Give the position of every malaria parasite.
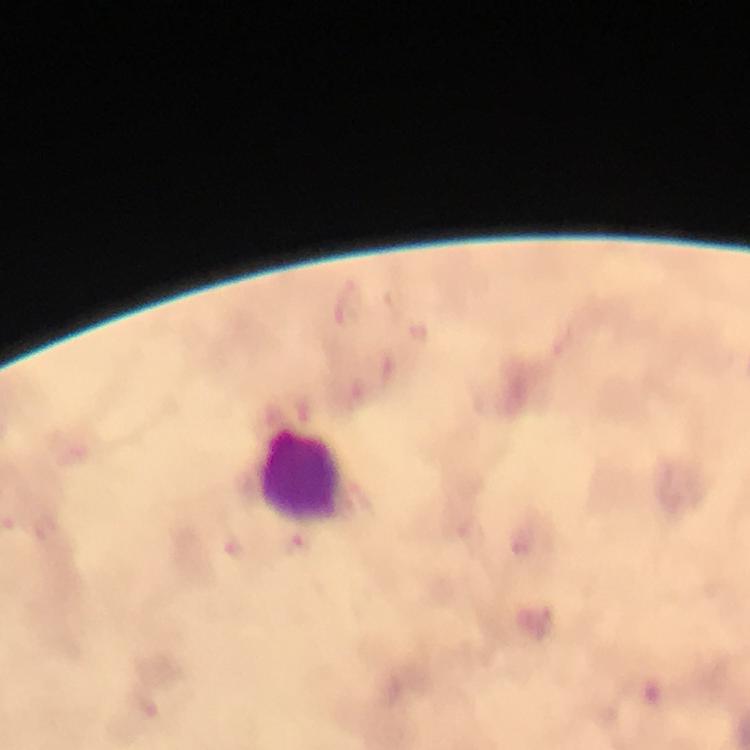

Approximate centers as (x, y) in pixels.
Malaria parasites: (298, 547).

Summary:
  - Leukocyte locations: (303, 474)
  - Image size: 750×750 pixels
  - Magnification: 100x
  - Cropped from: one field of view
  - Immersion oil: used
  - Preparation: thick blood film
  - Stain: Giemsa
  - Context: from a diagnostic examination for malaria
  - Capture: smartphone camera through the microscope